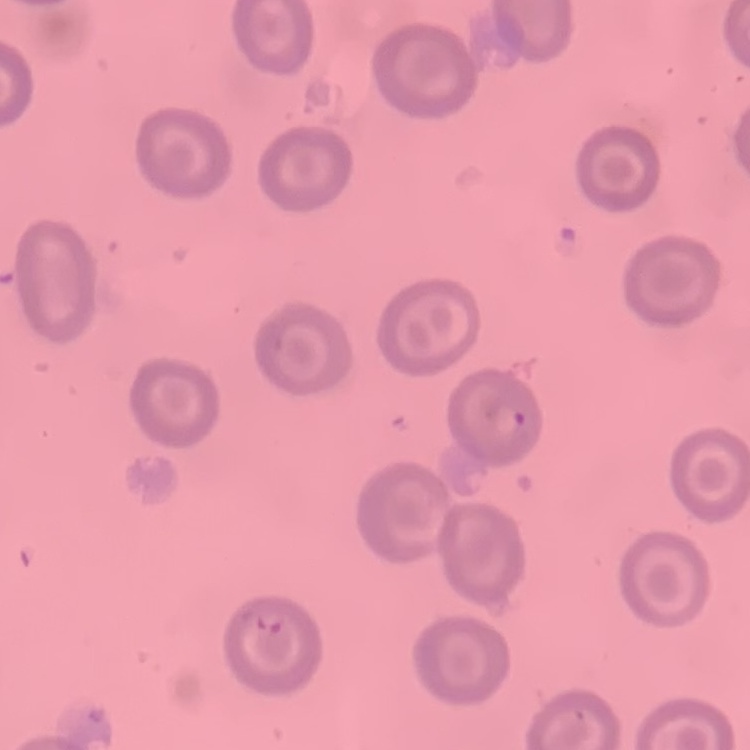
The red blood cells exhibit no rouleaux formation. Thin blood film. One tile cut from a larger photomicrograph. Stained with either Field's or Giemsa.